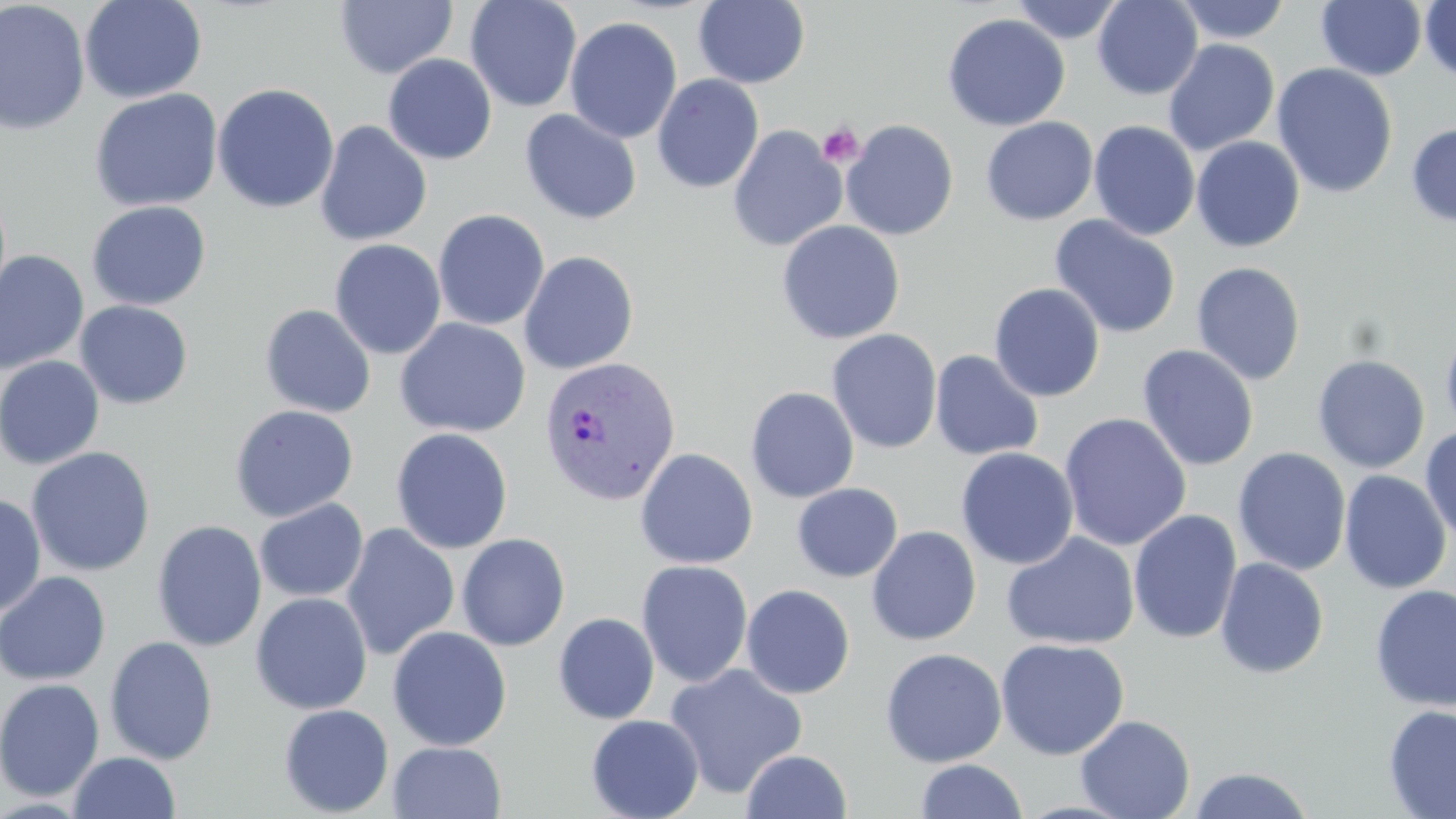

{
  "plasmodium_vivax_infected_red_blood_cell_locations": "approximate bounding boxes as named x1/y1/x2/y2 corners in pixels: (x1=538, y1=355, x2=680, y2=507)",
  "slide_level_diagnosis": "Plasmodium vivax",
  "field_of_view": "one of a larger specimen",
  "image_size": "1456×819 pixels",
  "uninfected_red_blood_cell_locations": "approximate bounding boxes as named x1/y1/x2/y2 corners in pixels: (x1=0, y1=0, x2=91, y2=136), (x1=79, y1=0, x2=207, y2=104), (x1=465, y1=0, x2=582, y2=113), (x1=1010, y1=0, x2=1126, y2=44), (x1=1093, y1=0, x2=1202, y2=99), (x1=1172, y1=0, x2=1292, y2=44), (x1=335, y1=1, x2=457, y2=79), (x1=694, y1=1, x2=810, y2=88), (x1=1315, y1=1, x2=1427, y2=81), (x1=1420, y1=1, x2=1455, y2=83), (x1=1298, y1=3, x2=1418, y2=162), (x1=942, y1=13, x2=1070, y2=132), (x1=565, y1=16, x2=682, y2=143), (x1=1163, y1=39, x2=1280, y2=156), (x1=383, y1=54, x2=497, y2=165), (x1=1271, y1=62, x2=1398, y2=198), (x1=651, y1=74, x2=764, y2=194), (x1=212, y1=83, x2=340, y2=214), (x1=89, y1=88, x2=223, y2=212), (x1=519, y1=109, x2=642, y2=225), (x1=981, y1=116, x2=1098, y2=226), (x1=841, y1=119, x2=959, y2=241), (x1=314, y1=120, x2=432, y2=246), (x1=1088, y1=121, x2=1200, y2=241), (x1=1406, y1=122, x2=1456, y2=228), (x1=728, y1=125, x2=847, y2=252), (x1=1190, y1=136, x2=1305, y2=252), (x1=86, y1=200, x2=211, y2=310), (x1=432, y1=209, x2=549, y2=331), (x1=1049, y1=215, x2=1181, y2=339), (x1=776, y1=220, x2=904, y2=344), (x1=329, y1=239, x2=446, y2=360), (x1=518, y1=250, x2=639, y2=374), (x1=0, y1=251, x2=89, y2=375), (x1=1191, y1=262, x2=1306, y2=385), (x1=989, y1=282, x2=1105, y2=402), (x1=75, y1=300, x2=193, y2=409), (x1=259, y1=304, x2=376, y2=418), (x1=394, y1=317, x2=531, y2=438), (x1=1440, y1=318, x2=1456, y2=443), (x1=826, y1=329, x2=942, y2=454), (x1=1137, y1=345, x2=1258, y2=471), (x1=929, y1=350, x2=1045, y2=462), (x1=1312, y1=354, x2=1430, y2=473), (x1=0, y1=356, x2=105, y2=470), (x1=745, y1=386, x2=859, y2=503), (x1=229, y1=404, x2=359, y2=522), (x1=1059, y1=413, x2=1192, y2=551), (x1=1420, y1=425, x2=1456, y2=547), (x1=390, y1=427, x2=513, y2=554), (x1=26, y1=446, x2=155, y2=577), (x1=955, y1=447, x2=1078, y2=570), (x1=1232, y1=447, x2=1351, y2=576), (x1=635, y1=448, x2=758, y2=569), (x1=1339, y1=470, x2=1452, y2=594), (x1=792, y1=483, x2=903, y2=582), (x1=0, y1=494, x2=47, y2=619), (x1=254, y1=499, x2=368, y2=602), (x1=1128, y1=509, x2=1243, y2=645), (x1=152, y1=520, x2=267, y2=652), (x1=340, y1=522, x2=460, y2=661), (x1=866, y1=526, x2=981, y2=645), (x1=1002, y1=532, x2=1139, y2=651), (x1=457, y1=533, x2=570, y2=651), (x1=1215, y1=557, x2=1329, y2=679), (x1=636, y1=559, x2=754, y2=687), (x1=0, y1=571, x2=111, y2=686), (x1=740, y1=584, x2=856, y2=699), (x1=1369, y1=584, x2=1456, y2=712), (x1=250, y1=592, x2=373, y2=715), (x1=553, y1=612, x2=660, y2=724), (x1=388, y1=625, x2=512, y2=751), (x1=104, y1=635, x2=219, y2=765), (x1=995, y1=638, x2=1129, y2=760), (x1=880, y1=647, x2=1007, y2=767), (x1=664, y1=663, x2=808, y2=799), (x1=0, y1=678, x2=105, y2=801), (x1=278, y1=704, x2=394, y2=817), (x1=1382, y1=705, x2=1456, y2=819), (x1=586, y1=714, x2=704, y2=819), (x1=1075, y1=715, x2=1195, y2=819), (x1=388, y1=741, x2=506, y2=819), (x1=741, y1=749, x2=852, y2=819), (x1=68, y1=751, x2=181, y2=819), (x1=915, y1=759, x2=1027, y2=818), (x1=1186, y1=766, x2=1316, y2=819)",
  "stain": "May-Grünwald-Giemsa",
  "platelet_locations": "approximate bounding boxes as named x1/y1/x2/y2 corners in pixels: (x1=817, y1=122, x2=864, y2=168)",
  "preparation": "thin blood smear",
  "magnification": "1000x",
  "modality": "light microscopy"
}